Classify this cell by malaria status.
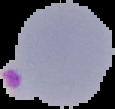

Parasitized.

preparation = thin blood film
image type = cell region segmented out of the field of view; surrounding area masked to black
image size = 115×109 pixels